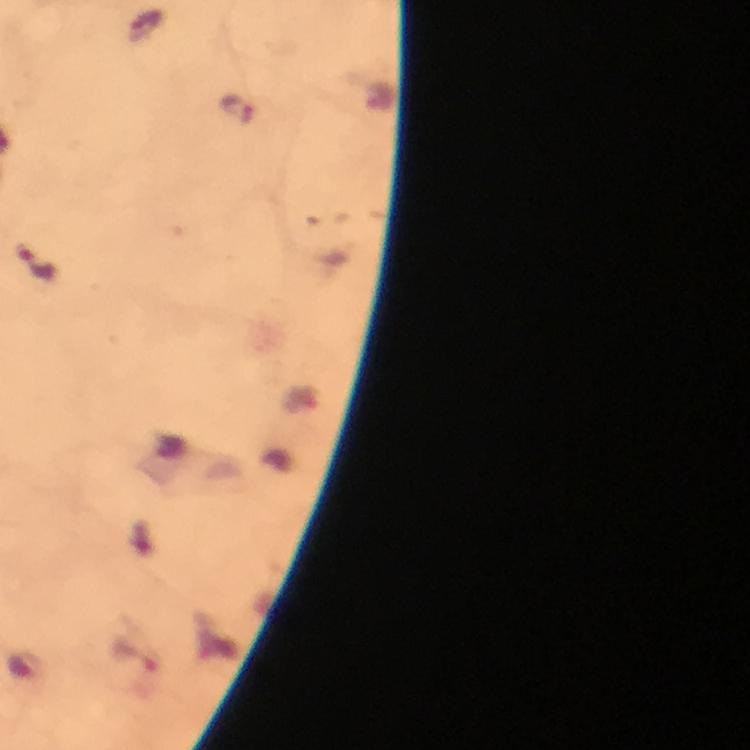
Approximate object centers, in pixels from the top-left corner. Malaria parasite locations: (x=236, y=109), (x=38, y=263). Giemsa stain. A crop from one field of view. Image is 750×750 pixels. At 100x magnification. Photographed through the microscope with a smartphone camera. From a malaria diagnostic workup. Immersion oil was used. Thick smear.